Identify the parasite.
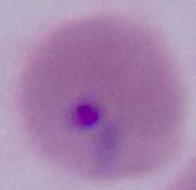
Plasmodium.

Summary:
  - Magnification: 400x or 1000x
  - Modality: photomicrograph